State the preparation type.
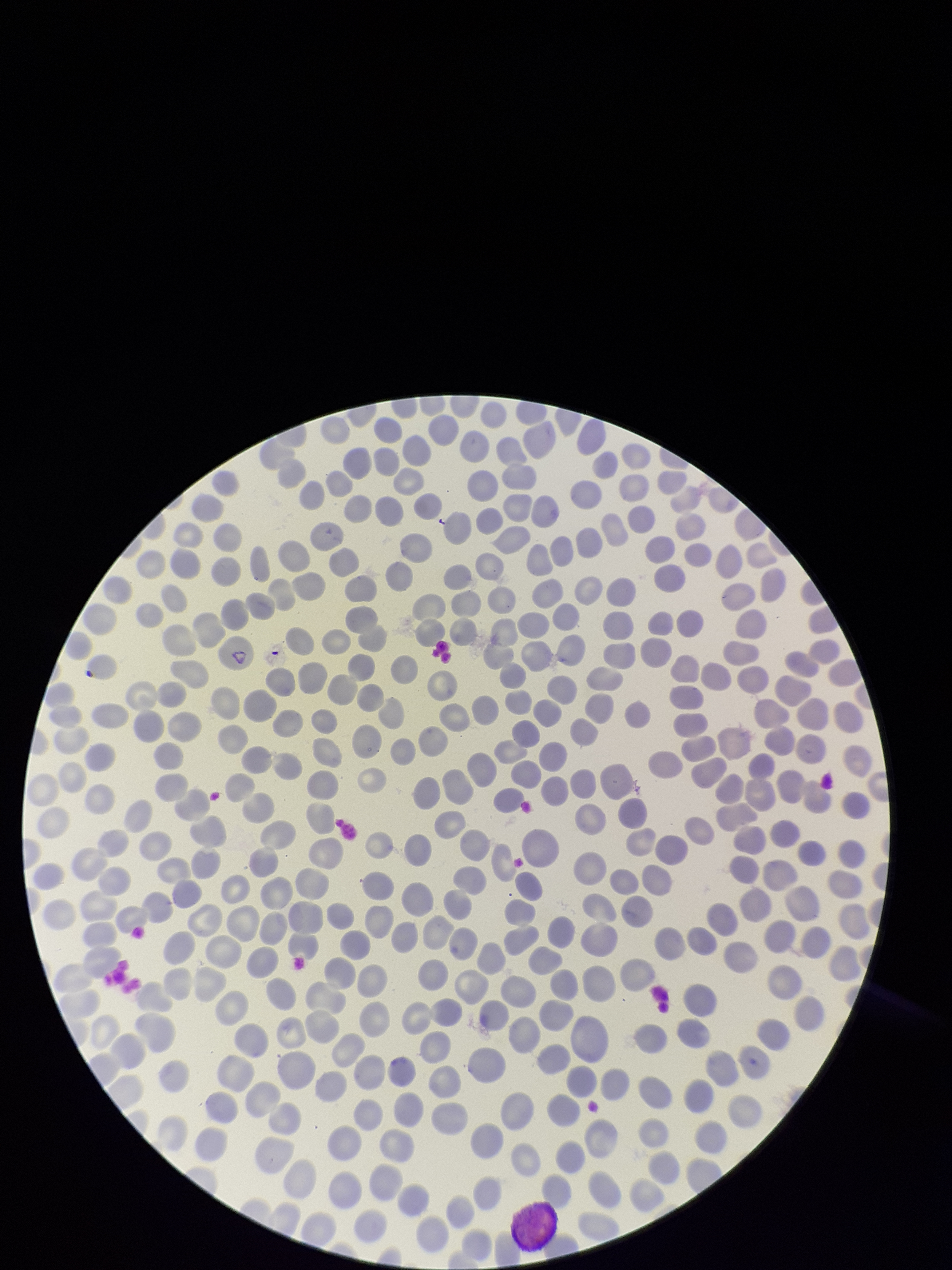

A thin smear.

field of view = single
stain = Giemsa
patient malaria status = positive
image size = 952×1270 pixels
red blood cell count = 329
parasitized red blood cells = none detected
parasitized red blood cell count = 0
capture = smartphone photograph through the microscope eyepiece
species reported for this patient = Plasmodium vivax